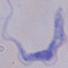

modality = photomicrograph
magnification = 1000x
identification = trypanosome